Outline each blood parasite and name the species.
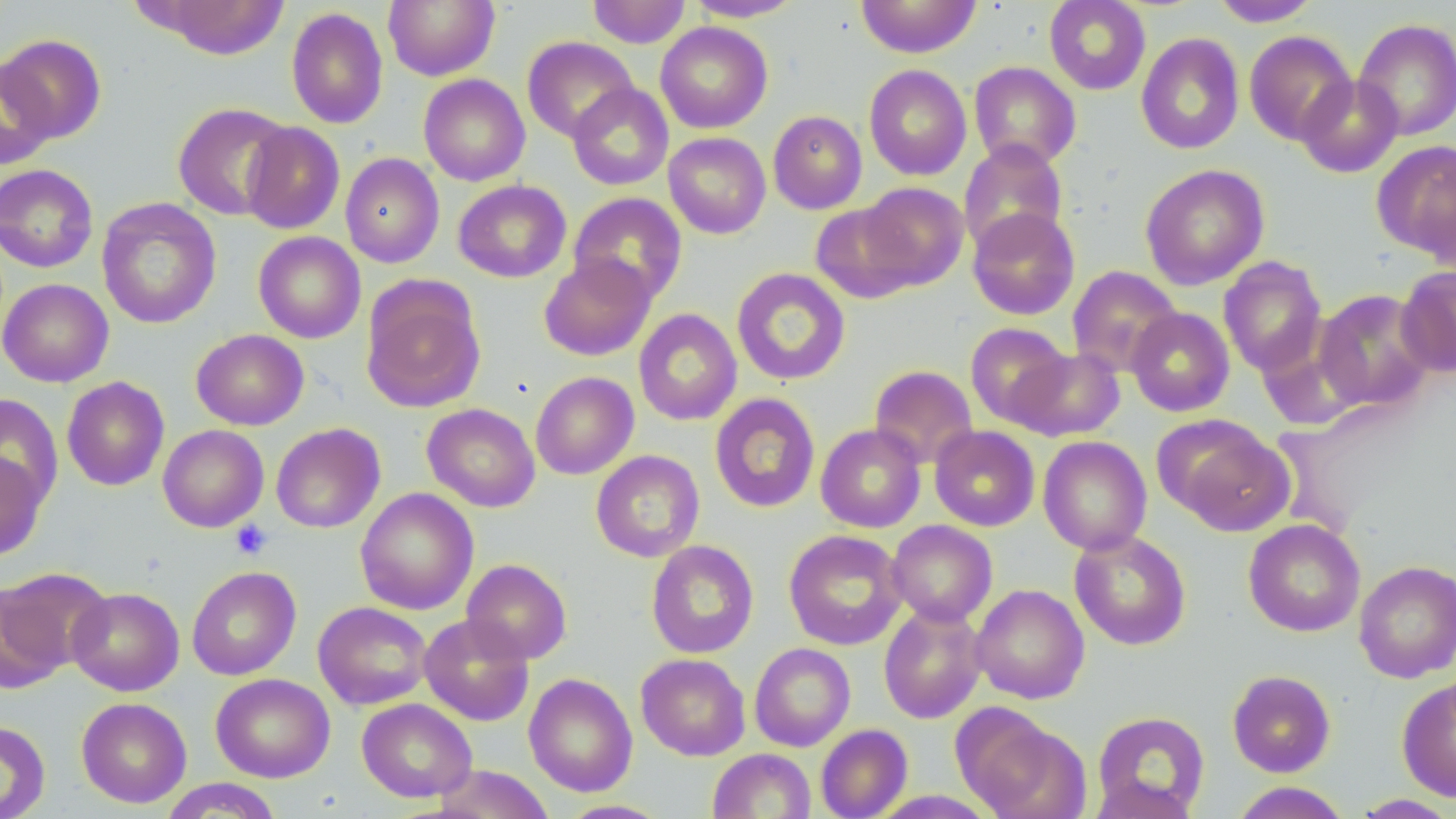

No blood parasites observed.

Summary:
  - Coordinate format: approximate bounding boxes as named x1/y1/x2/y2 corners in pixels
  - Uninfected red blood cell locations: (x1=383, y1=0, x2=500, y2=81), (x1=588, y1=0, x2=690, y2=48), (x1=686, y1=0, x2=804, y2=21), (x1=856, y1=0, x2=981, y2=58), (x1=1044, y1=0, x2=1151, y2=95), (x1=1209, y1=0, x2=1322, y2=27), (x1=147, y1=1, x2=290, y2=59), (x1=286, y1=7, x2=388, y2=129), (x1=1352, y1=18, x2=1456, y2=141), (x1=655, y1=21, x2=773, y2=133), (x1=1243, y1=30, x2=1357, y2=145), (x1=1135, y1=32, x2=1245, y2=154), (x1=1, y1=33, x2=107, y2=143), (x1=522, y1=36, x2=638, y2=142), (x1=0, y1=59, x2=56, y2=170), (x1=969, y1=61, x2=1081, y2=170), (x1=864, y1=65, x2=972, y2=180), (x1=418, y1=74, x2=530, y2=186), (x1=1295, y1=74, x2=1403, y2=178), (x1=567, y1=83, x2=673, y2=190), (x1=172, y1=102, x2=293, y2=221), (x1=768, y1=110, x2=867, y2=214), (x1=241, y1=122, x2=345, y2=234), (x1=664, y1=132, x2=771, y2=238), (x1=958, y1=140, x2=1069, y2=255), (x1=1371, y1=140, x2=1456, y2=261), (x1=340, y1=153, x2=444, y2=268), (x1=1140, y1=163, x2=1269, y2=290), (x1=0, y1=164, x2=98, y2=272), (x1=453, y1=179, x2=571, y2=283), (x1=859, y1=182, x2=969, y2=289), (x1=568, y1=192, x2=688, y2=304), (x1=96, y1=197, x2=221, y2=329), (x1=810, y1=203, x2=921, y2=304), (x1=967, y1=207, x2=1080, y2=320), (x1=253, y1=231, x2=366, y2=343), (x1=539, y1=254, x2=656, y2=361), (x1=1218, y1=256, x2=1327, y2=376), (x1=1396, y1=264, x2=1456, y2=378), (x1=1066, y1=265, x2=1183, y2=377), (x1=732, y1=268, x2=850, y2=385), (x1=1, y1=278, x2=114, y2=387), (x1=361, y1=281, x2=485, y2=414), (x1=1314, y1=288, x2=1436, y2=411), (x1=1126, y1=307, x2=1235, y2=416), (x1=634, y1=308, x2=742, y2=425), (x1=965, y1=322, x2=1072, y2=428), (x1=191, y1=329, x2=309, y2=430), (x1=1257, y1=335, x2=1364, y2=433), (x1=1010, y1=347, x2=1125, y2=441), (x1=869, y1=364, x2=978, y2=469), (x1=530, y1=371, x2=639, y2=479), (x1=61, y1=376, x2=169, y2=491), (x1=710, y1=393, x2=820, y2=513), (x1=0, y1=394, x2=63, y2=509), (x1=422, y1=403, x2=540, y2=512), (x1=1161, y1=418, x2=1293, y2=535), (x1=270, y1=422, x2=385, y2=533), (x1=816, y1=423, x2=926, y2=532), (x1=158, y1=425, x2=269, y2=532), (x1=929, y1=425, x2=1040, y2=531), (x1=1038, y1=435, x2=1152, y2=554), (x1=591, y1=450, x2=705, y2=562), (x1=0, y1=452, x2=48, y2=561), (x1=355, y1=487, x2=479, y2=615), (x1=1243, y1=518, x2=1365, y2=637), (x1=887, y1=520, x2=997, y2=626), (x1=783, y1=529, x2=908, y2=650), (x1=1069, y1=529, x2=1192, y2=650), (x1=646, y1=540, x2=759, y2=659), (x1=461, y1=559, x2=572, y2=664), (x1=1353, y1=560, x2=1456, y2=682), (x1=187, y1=566, x2=301, y2=680), (x1=0, y1=581, x2=71, y2=692), (x1=970, y1=584, x2=1089, y2=704), (x1=67, y1=587, x2=184, y2=696), (x1=313, y1=601, x2=432, y2=709), (x1=878, y1=602, x2=988, y2=723), (x1=419, y1=614, x2=535, y2=726), (x1=749, y1=643, x2=856, y2=751), (x1=636, y1=653, x2=751, y2=761), (x1=1227, y1=669, x2=1336, y2=777), (x1=211, y1=673, x2=335, y2=782), (x1=523, y1=673, x2=638, y2=797), (x1=1397, y1=677, x2=1456, y2=802), (x1=76, y1=697, x2=192, y2=807), (x1=357, y1=698, x2=476, y2=802), (x1=954, y1=705, x2=1088, y2=819), (x1=1092, y1=711, x2=1210, y2=817), (x1=0, y1=720, x2=50, y2=819), (x1=816, y1=724, x2=913, y2=819), (x1=707, y1=748, x2=816, y2=819), (x1=432, y1=764, x2=554, y2=819), (x1=1087, y1=775, x2=1200, y2=819), (x1=158, y1=778, x2=284, y2=818), (x1=1229, y1=782, x2=1352, y2=819), (x1=869, y1=789, x2=999, y2=819), (x1=1349, y1=794, x2=1456, y2=818), (x1=558, y1=799, x2=672, y2=818)
  - Platelet locations: (x1=230, y1=520, x2=272, y2=560)
  - Slide-level diagnosis: negative for blood parasites
  - Magnification: 1000x
  - Image size: 1456×819 pixels
  - Preparation: thin blood smear
  - Field of view: one of a larger specimen
  - Modality: light microscopy
  - Stain: May-Grünwald-Giemsa